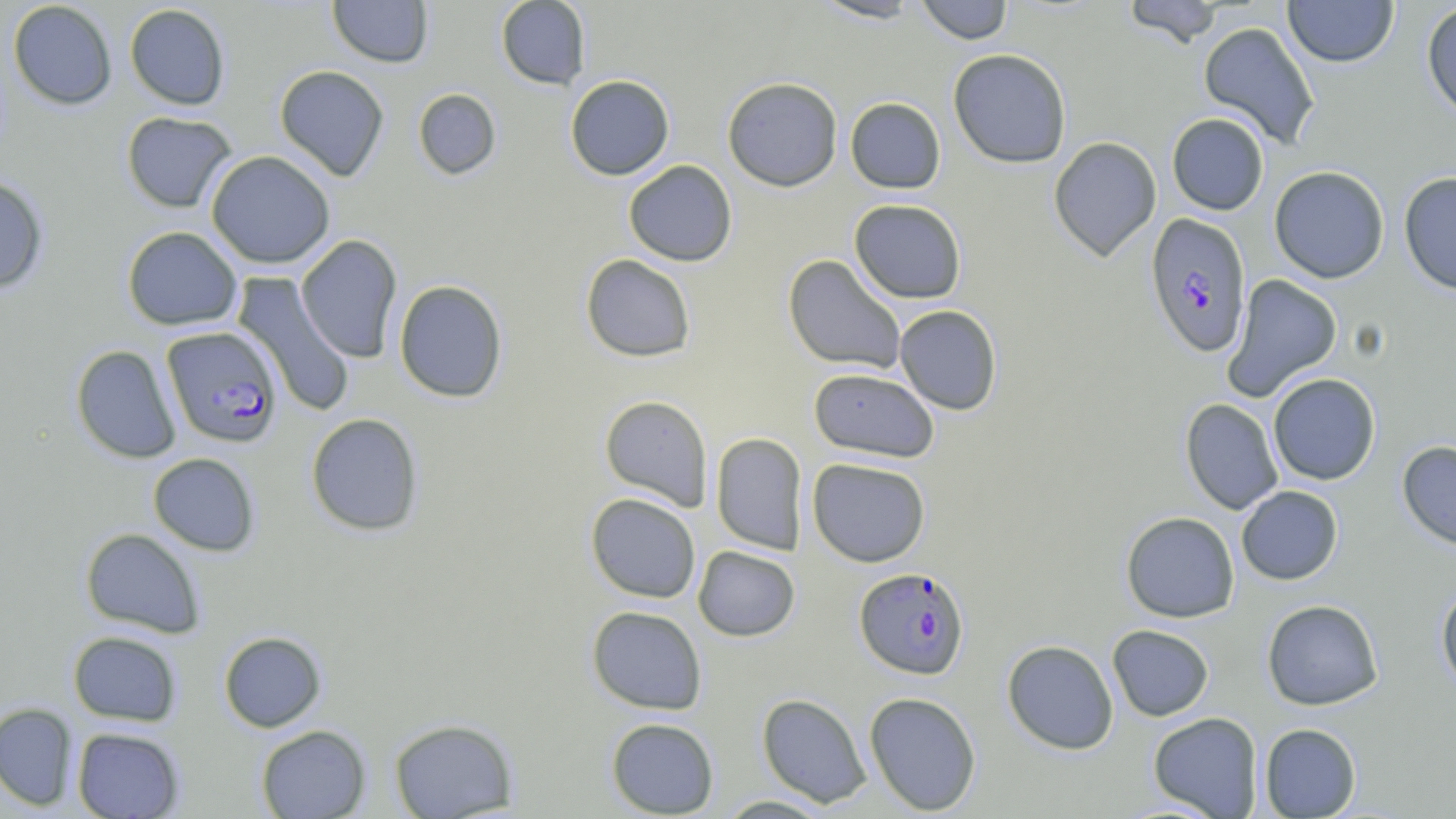
Summary:
  - Coordinate format: approximate bounding boxes as [x1, y1, x2, y2] in pixels
  - Plasmodium falciparum-infected red blood cell locations: [1145, 212, 1252, 357], [162, 326, 283, 448], [854, 566, 970, 680]
  - Uninfected red blood cell locations: [327, 0, 434, 68], [495, 0, 591, 90], [810, 0, 924, 23], [914, 0, 1013, 45], [1121, 0, 1226, 48], [1283, 0, 1399, 67], [8, 1, 118, 110], [1421, 2, 1456, 122], [124, 4, 231, 110], [1198, 21, 1321, 149], [948, 48, 1072, 168], [274, 65, 389, 181], [564, 75, 675, 181], [721, 76, 843, 192], [413, 88, 501, 180], [845, 97, 946, 194], [121, 111, 237, 214], [1166, 113, 1269, 215], [1048, 136, 1162, 262], [206, 150, 335, 269], [624, 160, 737, 266], [1269, 166, 1389, 283], [1398, 171, 1456, 296], [0, 175, 49, 293], [849, 199, 966, 303], [122, 226, 243, 331], [295, 234, 403, 363], [579, 254, 697, 362], [783, 254, 907, 374], [232, 271, 355, 417], [1222, 274, 1343, 401], [393, 279, 508, 402], [894, 305, 1003, 415], [71, 344, 181, 464], [808, 367, 940, 462], [1268, 373, 1381, 485], [599, 395, 713, 510], [1180, 398, 1283, 515], [306, 412, 425, 536], [710, 432, 808, 555], [1397, 440, 1456, 551], [148, 453, 260, 556], [807, 458, 931, 567], [1236, 485, 1343, 585], [585, 492, 701, 603], [1120, 511, 1239, 623], [80, 527, 206, 637], [693, 546, 800, 641], [1435, 583, 1456, 694], [1261, 599, 1383, 710], [586, 605, 708, 715], [1107, 624, 1214, 722], [67, 631, 182, 726], [218, 631, 327, 732], [1001, 639, 1119, 755], [864, 692, 982, 815], [756, 693, 872, 807], [0, 702, 79, 811], [1148, 712, 1263, 818], [388, 717, 519, 818], [605, 717, 720, 818], [1259, 723, 1361, 818], [255, 724, 372, 818], [72, 726, 185, 818], [714, 795, 835, 817]
  - Slide-level diagnosis: Plasmodium falciparum
  - Field of view: one of a larger specimen
  - Preparation: thin blood smear
  - Image size: 1456×819 pixels
  - Magnification: 1000x
  - Stain: May-Grünwald-Giemsa
  - Modality: optical microscopy